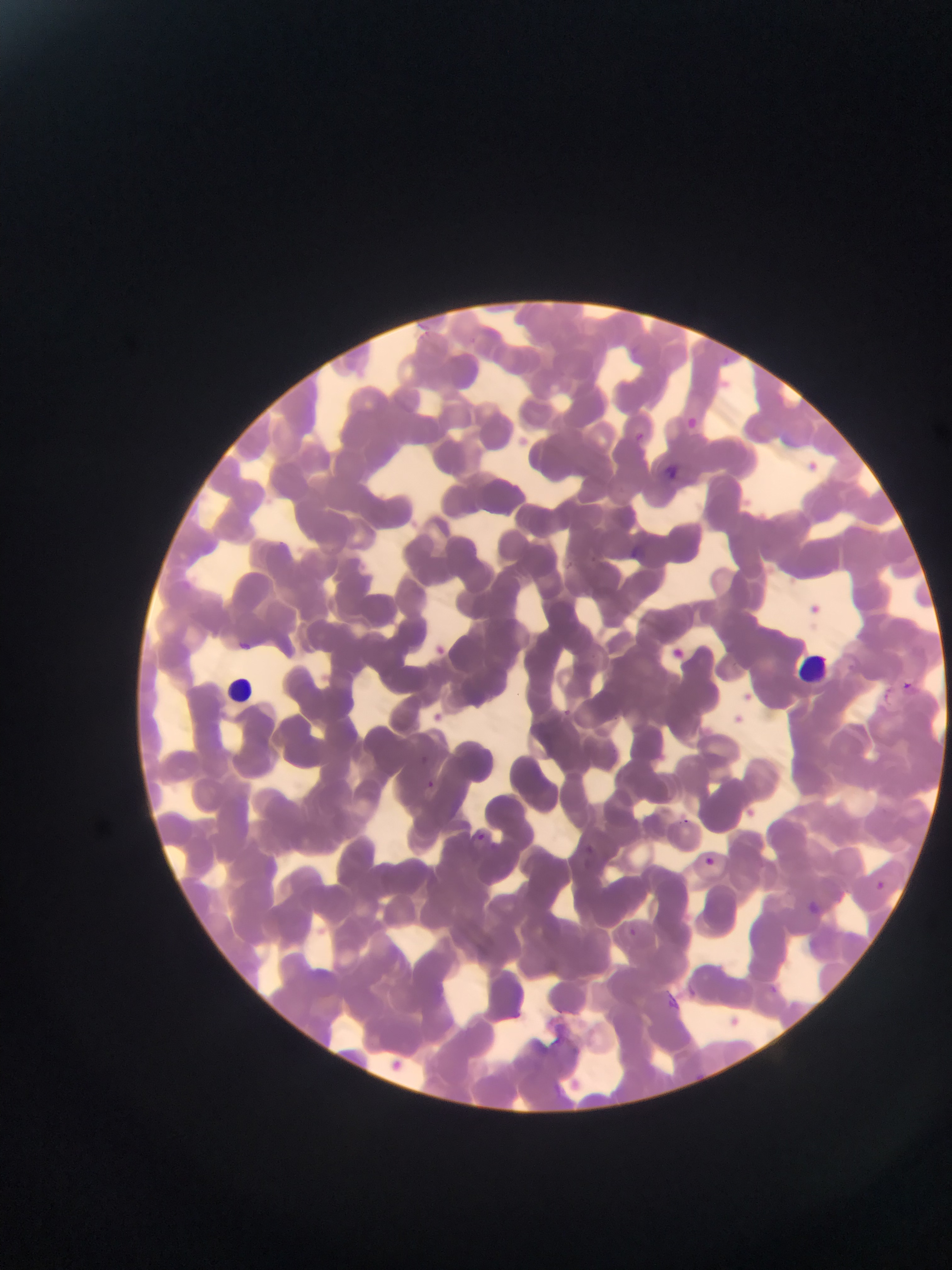
Approximate bounding boxes as left top right bottom in pixels.
Summary:
  - Leukocyte locations: 799 652 831 684; 228 678 253 705; 720 1012 745 1030; 393 1054 411 1072
  - Malaria parasite locations: 722 356 731 363; 687 415 699 427; 634 431 645 442; 804 458 825 480; 665 464 682 480; 630 543 643 556; 809 597 825 615; 237 640 255 653; 433 642 452 659; 672 646 689 662; 903 680 913 689; 745 688 762 704; 733 706 754 726; 561 707 571 717; 433 709 454 728; 420 754 429 764; 426 778 436 789; 738 807 755 820; 476 830 486 840; 585 842 596 855; 705 856 716 866; 876 881 885 889; 807 900 823 916; 628 926 637 935; 767 983 778 994; 686 986 698 998; 662 989 683 1011
  - Country: Ghana
  - Field of view: single
  - Preparation: thin blood smear
  - Image size: 952×1270 pixels
  - Capture: mobile-phone photograph through a microscope